Give the extent of all uninfected red blood cells.
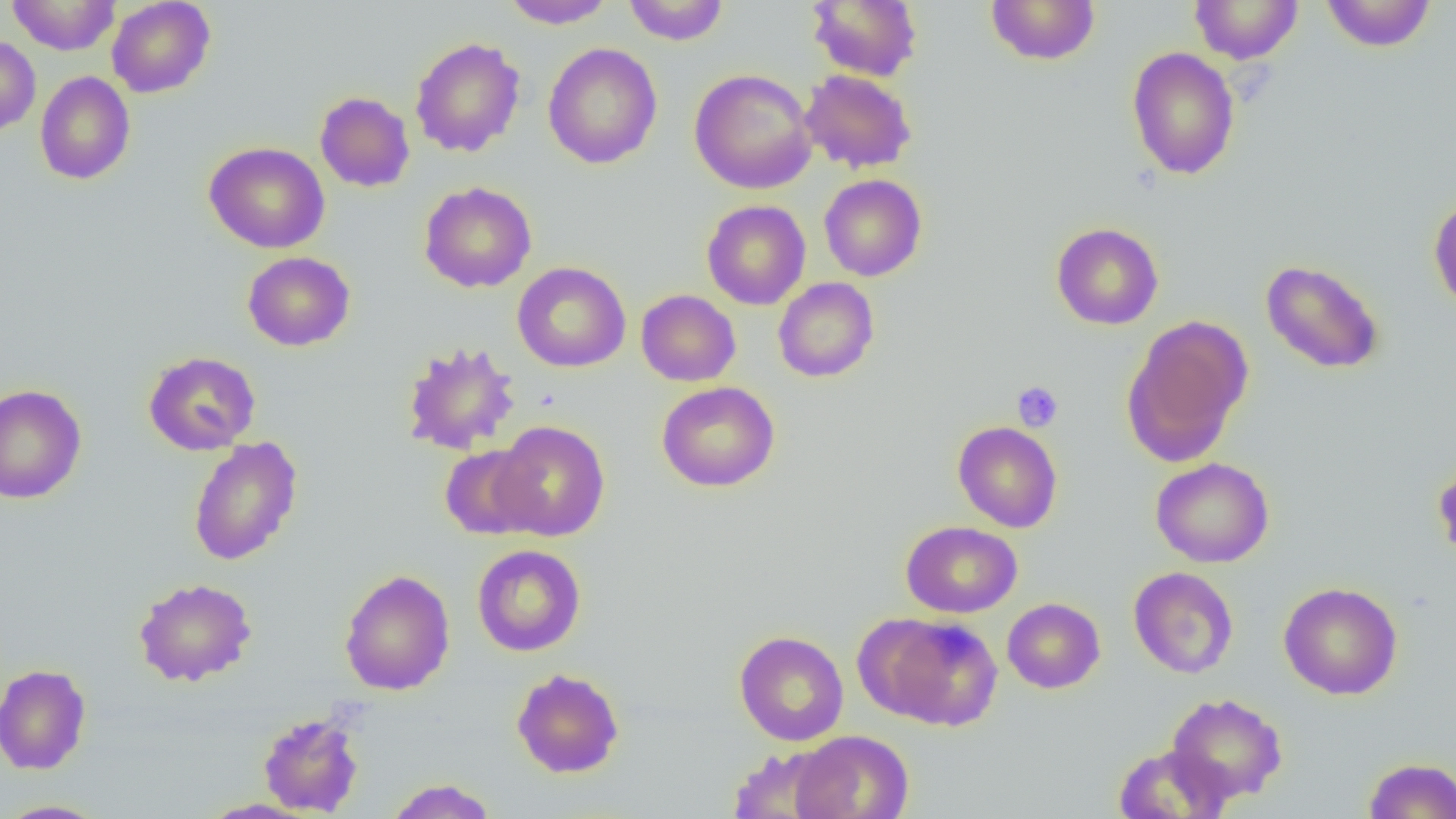
Approximate bounding boxes as (x1,y1)-(x2,y2) corner pairs in pixels.
Uninfected red blood cells: (7,0)-(120,55), (106,0)-(215,98), (500,0)-(617,29), (623,0)-(728,45), (985,0)-(1101,66), (1321,0)-(1436,52), (807,1)-(921,81), (1189,1)-(1304,64), (0,35)-(41,136), (410,37)-(526,158), (542,43)-(662,169), (1126,47)-(1240,180), (689,68)-(817,194), (799,69)-(917,173), (34,71)-(136,185), (315,91)-(415,192), (204,141)-(331,253), (819,174)-(927,281), (419,181)-(537,293), (1428,196)-(1456,313), (702,200)-(811,309), (1050,222)-(1164,330), (242,251)-(355,351), (1260,259)-(1385,374), (512,262)-(631,373), (773,277)-(879,382), (636,289)-(740,386), (1122,316)-(1252,466), (401,341)-(522,456), (143,351)-(260,455), (657,381)-(780,492), (0,384)-(87,504), (491,420)-(611,541), (952,421)-(1063,533), (188,436)-(303,566), (439,444)-(543,540), (1150,457)-(1275,568), (1432,458)-(1456,564), (900,521)-(1022,617), (472,544)-(586,656), (1128,566)-(1238,679), (339,569)-(455,695), (133,577)-(257,687), (1278,581)-(1403,700), (1002,598)-(1105,693), (867,613)-(1004,730), (734,630)-(849,745), (0,663)-(91,775), (511,668)-(625,779), (1165,692)-(1288,805), (258,711)-(364,816), (789,730)-(914,819), (1112,744)-(1232,819), (728,746)-(839,819), (1363,757)-(1456,818), (384,778)-(498,818), (199,798)-(317,818), (0,799)-(111,818).

Summary:
  - Platelet locations: (1012,381)-(1064,432)
  - Slide-level diagnosis: no evidence of blood parasites
  - Modality: optical microscopy
  - Field of view: one of a larger specimen
  - Image size: 1456×819 pixels
  - Preparation: thin blood smear
  - Magnification: 1000x